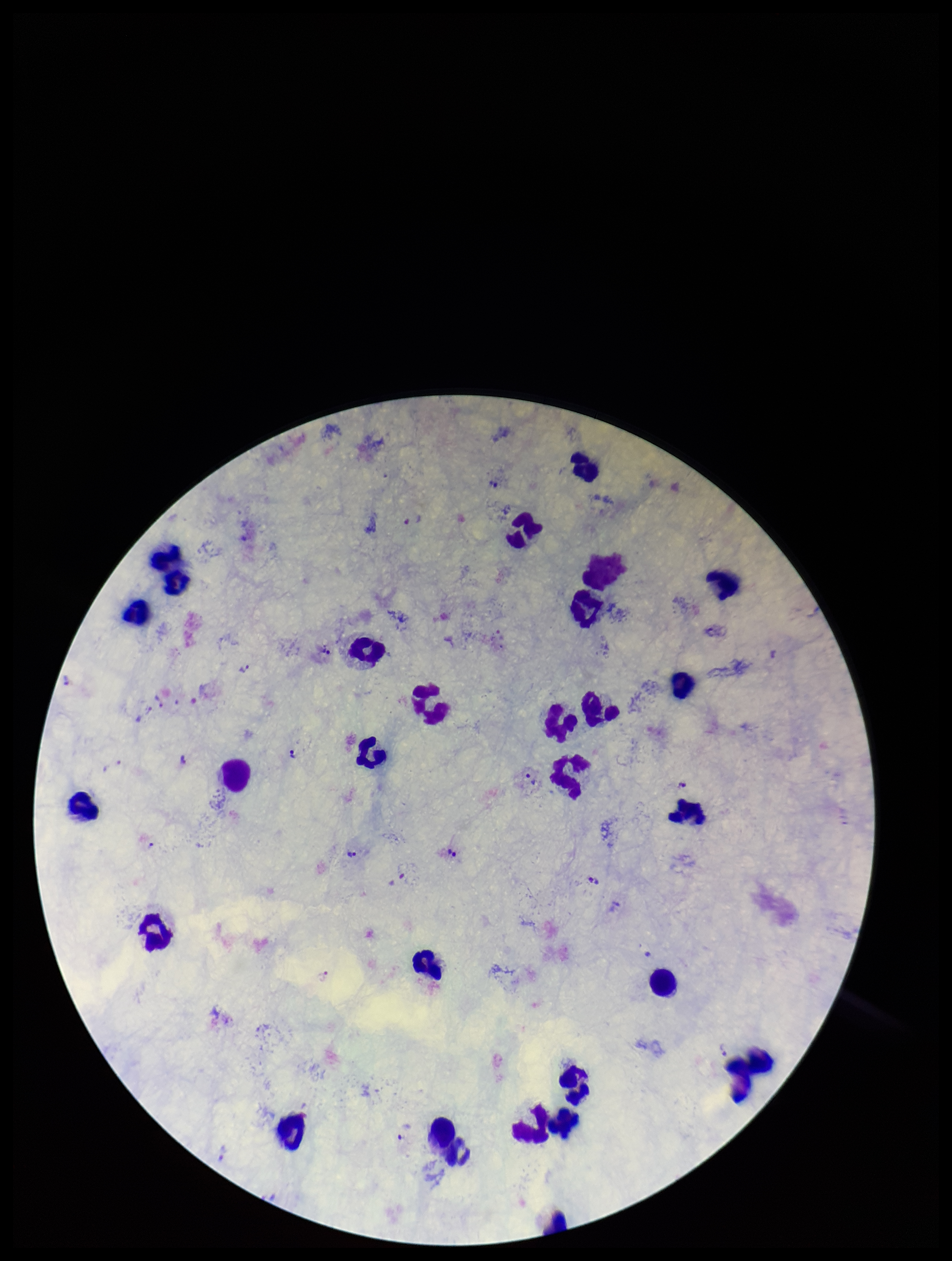
parasite count = 17
Plasmodium parasites = detected
image size = 952×1261 pixels
field of view = single
capture = smartphone photograph through the microscope eyepiece
preparation = thick blood smear
leukocyte count = 24
stain = Giemsa
patient malaria status = infected
species reported for this patient = Plasmodium vivax